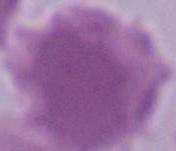

identification: red blood cell
modality: micrograph
magnification: 1000x